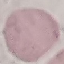

{
  "malaria_status": "uninfected",
  "preparation": "thin blood smear",
  "stain": "Giemsa",
  "capture": "smartphone through the microscope eyepiece",
  "image_type": "automatically extracted cell patch, resized to 64 × 64 pixels"
}